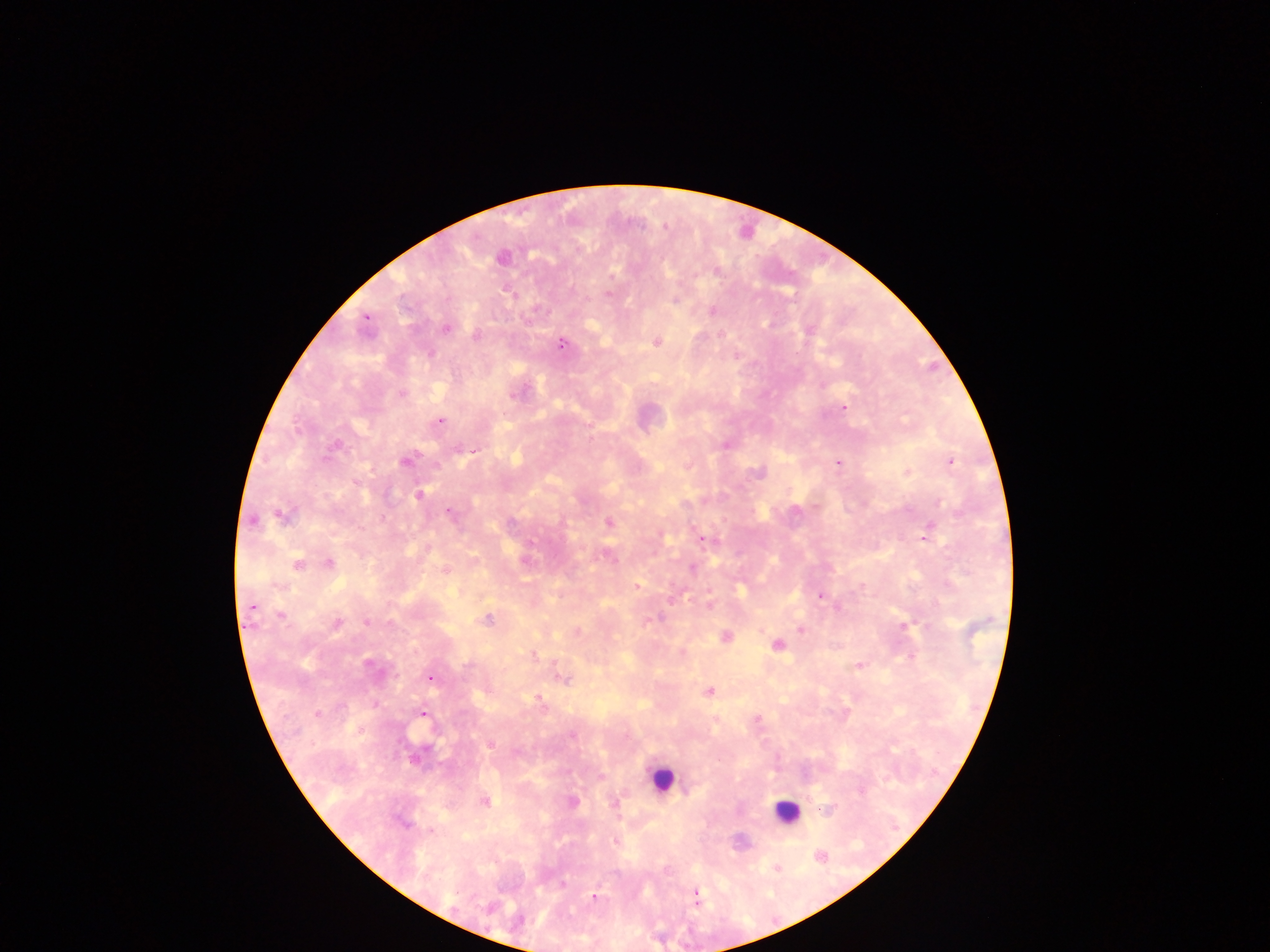 Approximate centers as x y in pixels. Leukocyte locations: 661 778; 786 812. Malaria parasite locations: 502 257; 716 271; 608 294; 675 301; 712 311; 366 318; 446 329; 477 336; 656 342; 562 344; 401 395; 513 395; 843 407; 440 421; 725 445; 334 446; 457 449; 474 451; 405 461; 950 461; 838 463; 757 473; 356 482; 419 494; 448 512; 281 515; 252 520; 511 523; 609 523; 925 537; 703 540; 530 542; 526 561; 329 562; 297 565; 693 569; 445 571; 636 587; 820 596; 688 601; 710 604; 251 606; 281 616; 487 618; 650 620; 366 622; 337 623; 904 626; 801 629; 577 632; 725 636; 777 645; 682 653; 534 656; 909 656; 368 664; 859 666; 430 679; 564 680; 710 692; 537 698; 540 703; 317 714; 423 714; 758 719; 360 729; 572 735; 491 745; 485 801; 573 801; 615 803; 431 831; 614 841; 819 856; 562 885; 594 897; 695 897. Thick blood film. Sample from Ghana. One field of view. Mobile-phone photograph taken through the microscope. Image is 1270×952 pixels.